Assess this cell for malaria.
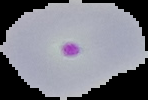

It is parasitized.

preparation = thin blood film
image size = 148×100 pixels
image type = segmented cell region with the area outside set to black